State the preparation type.
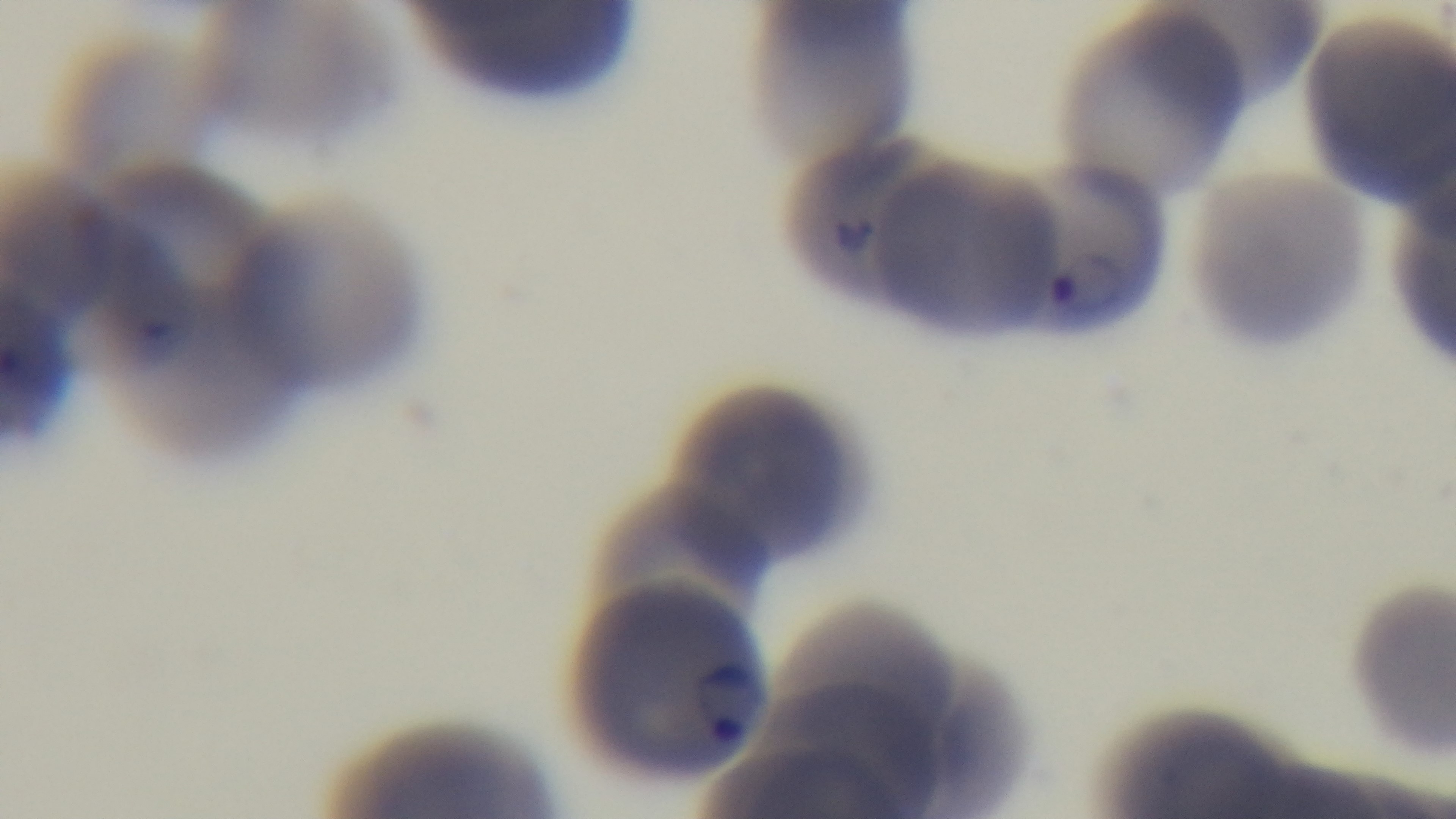

It is a thin blood film.

One field from the slide. 100x oil-immersion objective. Light microscopy. Malaria status: infected. Giemsa-stained. Mounted 4K digital camera.